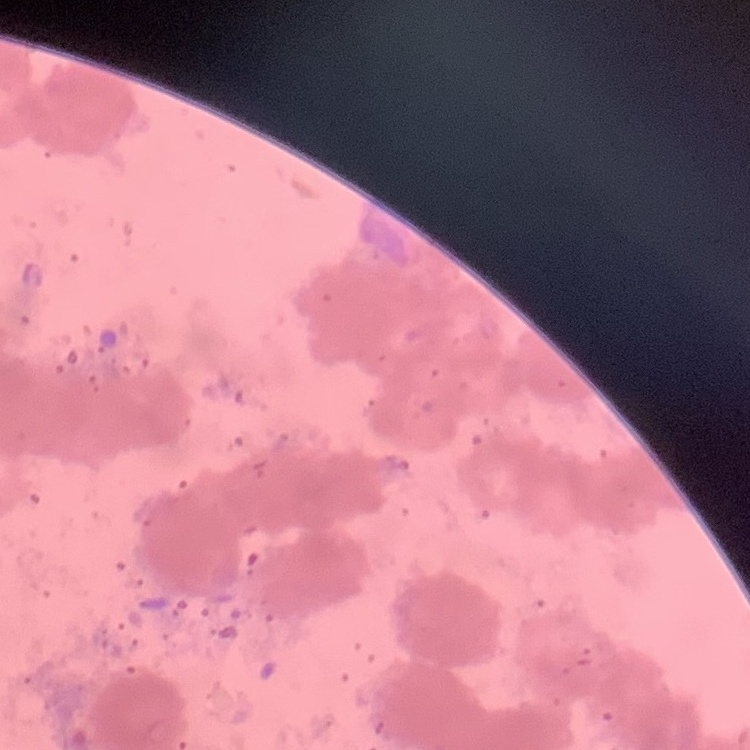
Summary:
  - Erythrocyte morphology: rouleaux formation
  - Image type: square crop of a larger photomicrograph
  - Preparation: thin blood film
  - Stain: Field's or Giemsa